Identify the parasite.
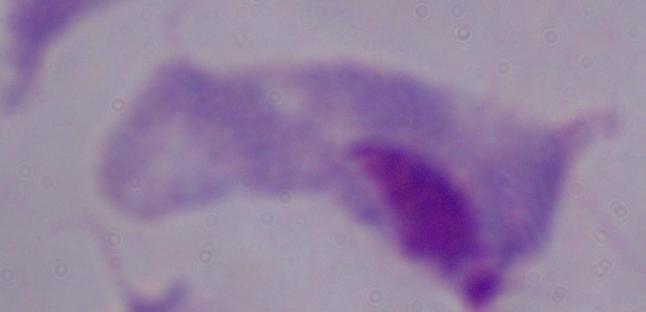
A trichomonad.

{
  "modality": "micrograph",
  "magnification": "1000x"
}